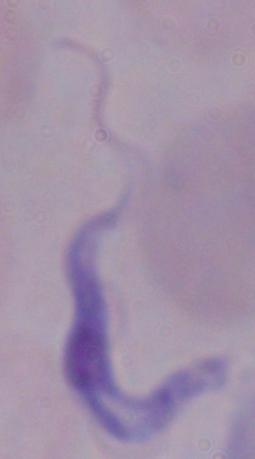
Captured at 1000x magnification. A trypanosome is shown. Photomicrograph.